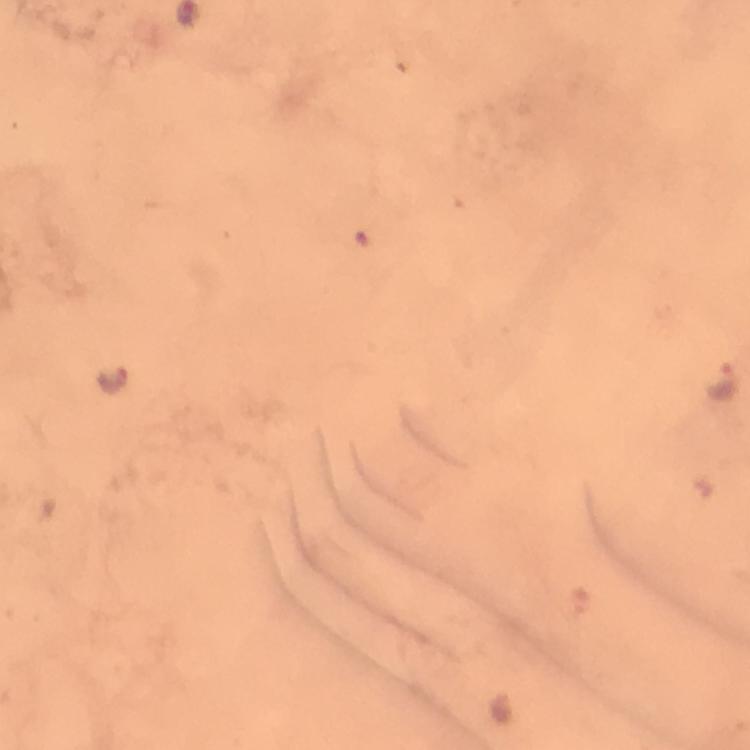
Approximate centers as (x, y) in pixels.
Summary:
  - Plasmodium parasite locations: (110, 380), (722, 380)
  - Capture: smartphone photograph through a microscope
  - Stain: Giemsa
  - Context: from a malaria diagnostic workup
  - Preparation: thick blood film
  - Image size: 750×750 pixels
  - Cropped from: a single field of view
  - Magnification: 100x
  - Immersion oil: used